Classify this cell by malaria status.
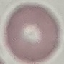
It is uninfected.

Summary:
  - Image type: cell patch, automatically extracted from a larger field of view and resized to 64 × 64 pixels
  - Preparation: thin blood smear
  - Capture: smartphone through the microscope eyepiece
  - Stain: Giemsa